Report the malaria status of this cell.
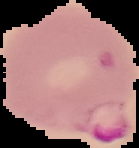

It is parasitized.

Image is 139×148 pixels. Cell region segmented out of the field of view; the surrounding area is masked to black. From a thin blood film.